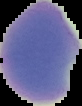 The area outside the segmented cell region is set to black. From a thin blood smear. Malaria status: uninfected. Image is 82×106 pixels.